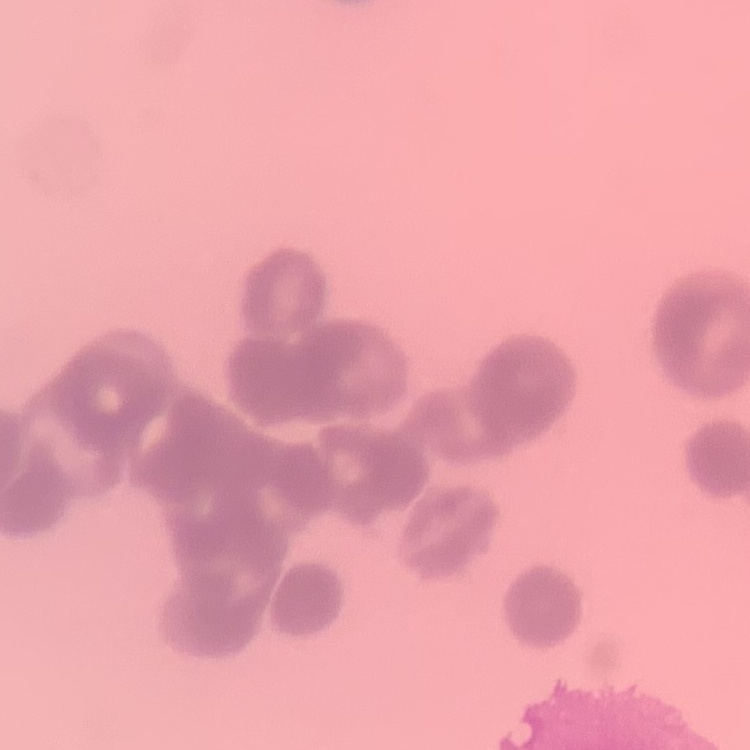

The red blood cells exhibit rouleaux formation. Stained with either Field's or Giemsa. Square crop of a larger photomicrograph. Thin peripheral smear.